Identify the parasite.
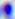

This is Toxoplasma gondii.

{
  "magnification": "400x",
  "modality": "micrograph"
}